Report the malaria status of this cell.
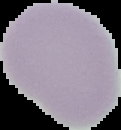
It is uninfected.

preparation: thin blood film
image_size: 121×130 pixels
image_type: segmented cell region with the area outside set to black